Assess this cell for malaria.
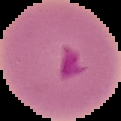
It is parasitized.

image_type: segmented cell region with the area outside set to black
image_size: 121×121 pixels
preparation: thin blood smear